Name the parasite shown.
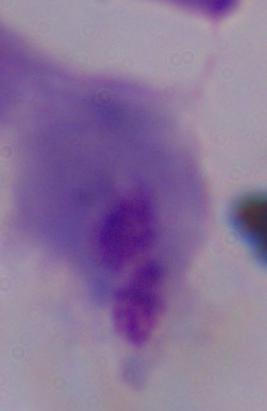
This is a trichomonad.

magnification = 1000x
modality = micrograph